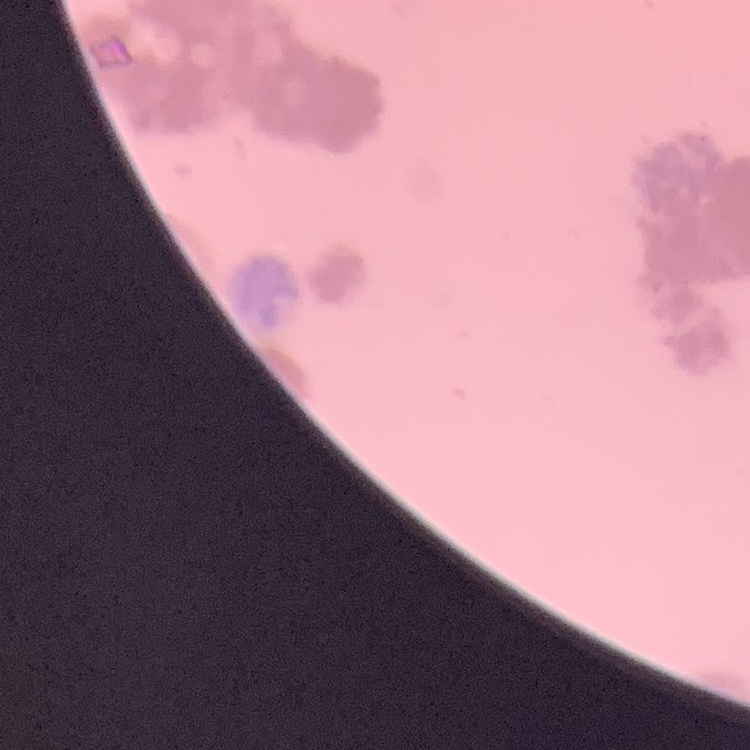
erythrocyte morphology = rouleaux formation
preparation = thin peripheral smear
stain = Field's or Giemsa
image type = one tile cut from a larger photomicrograph